Give the position of every malaria parasite.
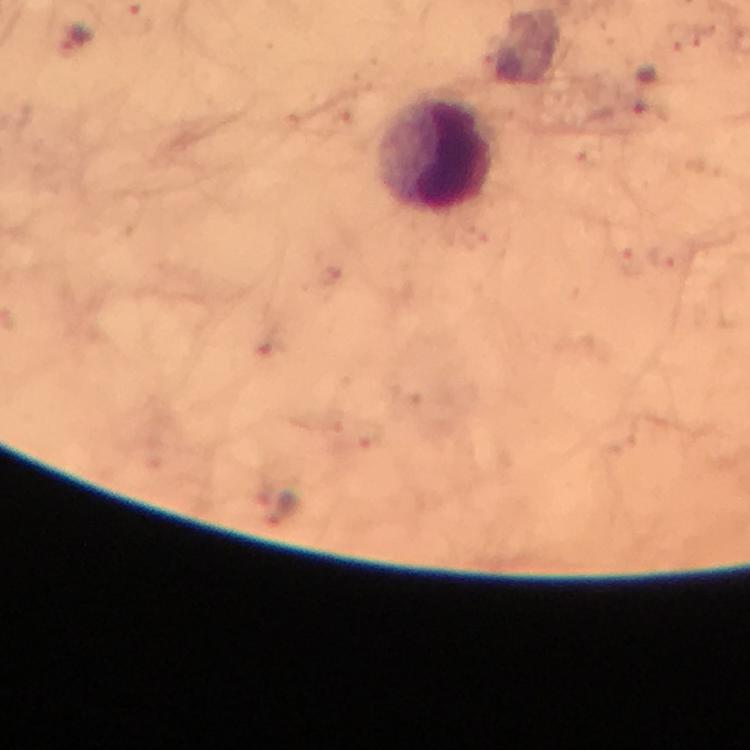

Approximate centers as [x, y] in pixels.
Malaria parasites: [137, 20], [283, 512].

Summary:
  - Leukocyte locations: [437, 154]
  - Image size: 750×750 pixels
  - Preparation: thick blood film
  - Magnification: 100x
  - Immersion oil: used
  - Stain: Giemsa
  - Cropped from: a single field of view
  - Context: from a malaria diagnostic workup
  - Capture: smartphone mounted on the microscope